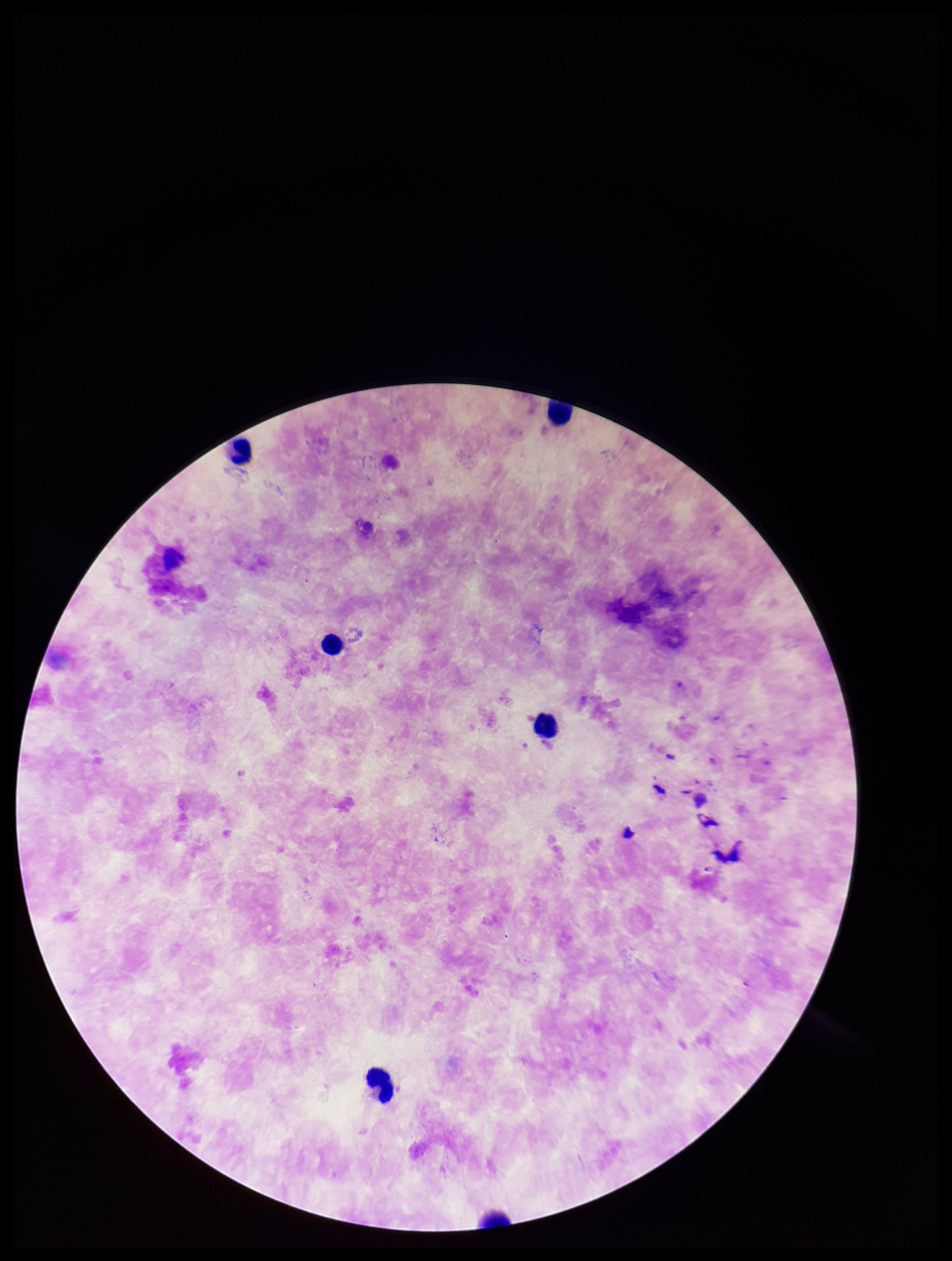

Summary:
  - Patient malaria status: infected
  - Capture: smartphone photograph through the microscope eyepiece
  - Species reported for this patient: Plasmodium falciparum
  - Image size: 952×1261 pixels
  - Leukocyte count: 6
  - Field of view: single
  - Parasite count: 0
  - Stain: Giemsa
  - Preparation: thick blood smear
  - Plasmodium parasites: none identified